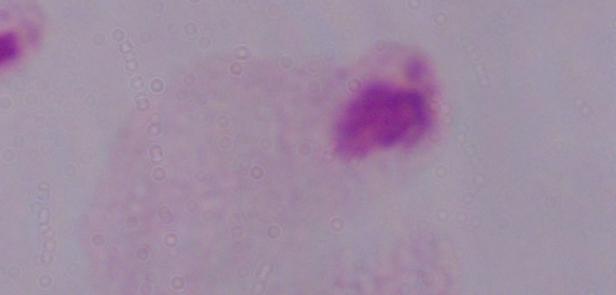 Photomicrograph. Captured at 1000x magnification. A trichomonad is seen.